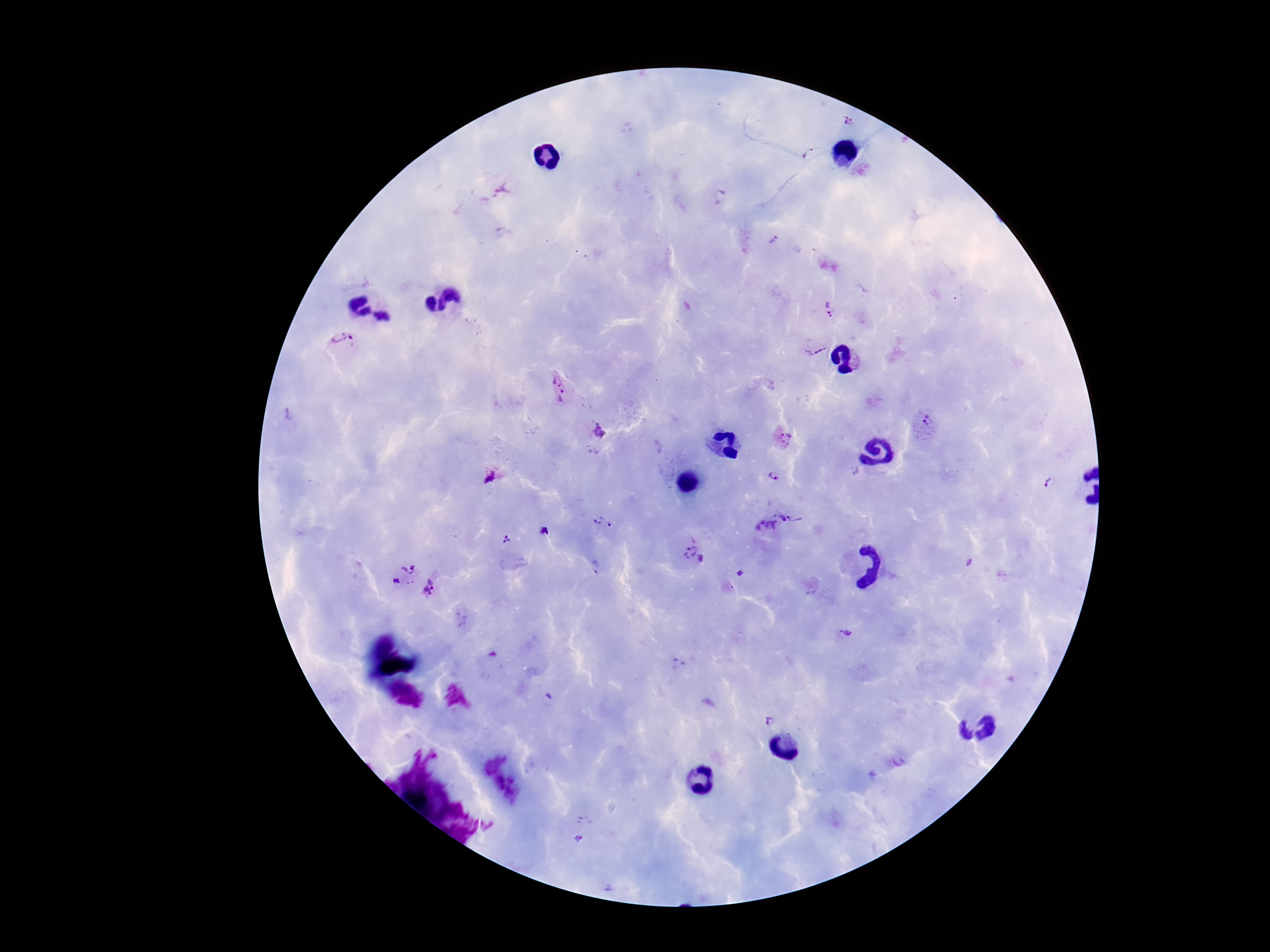
Approximate centers as (x, y) in pixels. Plasmodium parasite locations: (849, 119), (812, 155), (720, 197), (771, 241), (828, 309), (344, 342), (816, 348), (558, 388), (926, 423), (598, 431), (783, 439), (492, 475), (773, 476), (1051, 484), (775, 522), (602, 524), (506, 538), (690, 550), (701, 560), (597, 567), (405, 574), (432, 589), (844, 634), (678, 666), (769, 721), (581, 837). Image is 1270×952 pixels. One field from this slide. Patient malaria status: infected. Giemsa-stained preparation. Photographed through the microscope eyepiece with a smartphone camera. Thick blood film. 100x magnification.